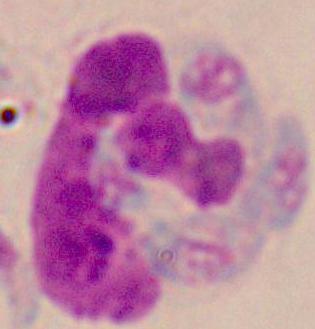

Summary:
  - Modality: micrograph
  - Magnification: 1000x
  - Identification: white blood cell